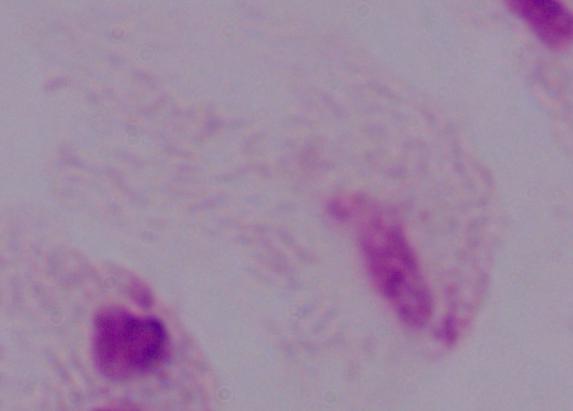

Summary:
  - Modality: micrograph
  - Identification: trichomonad
  - Magnification: 1000x